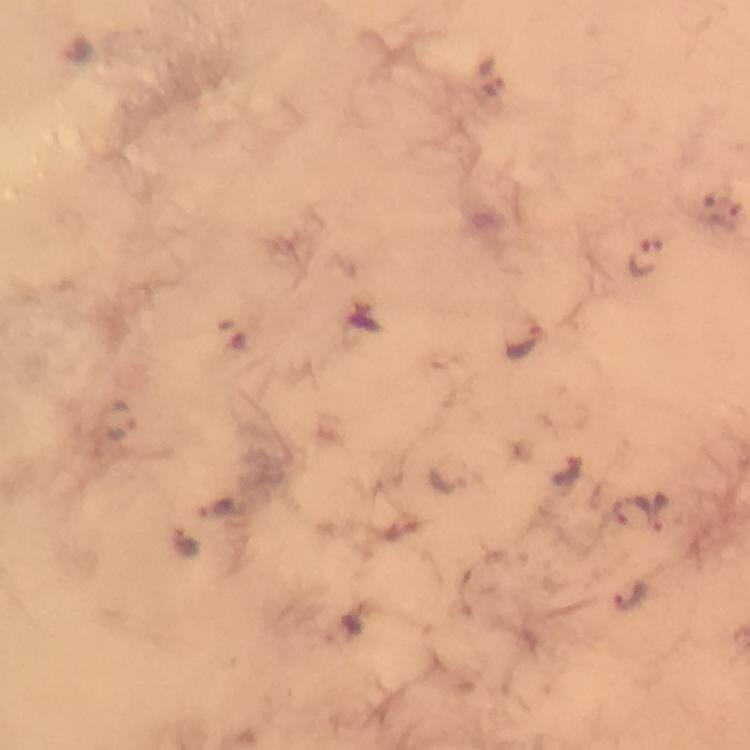
Approximate centers as [x, y] in pixels. Plasmodium parasite locations: [74, 49], [493, 76], [728, 220], [645, 257], [520, 339], [119, 421], [217, 509], [660, 514], [630, 516], [185, 550], [632, 598], [342, 627]. From a diagnostic examination for malaria. Photographed through the microscope with a smartphone camera. At 100x magnification. Image is 750×750 pixels. Thick blood smear. Immersion oil applied. Cropped region of a single field of view. Giemsa stain.